Give the position of every Plasmodium parasite visible.
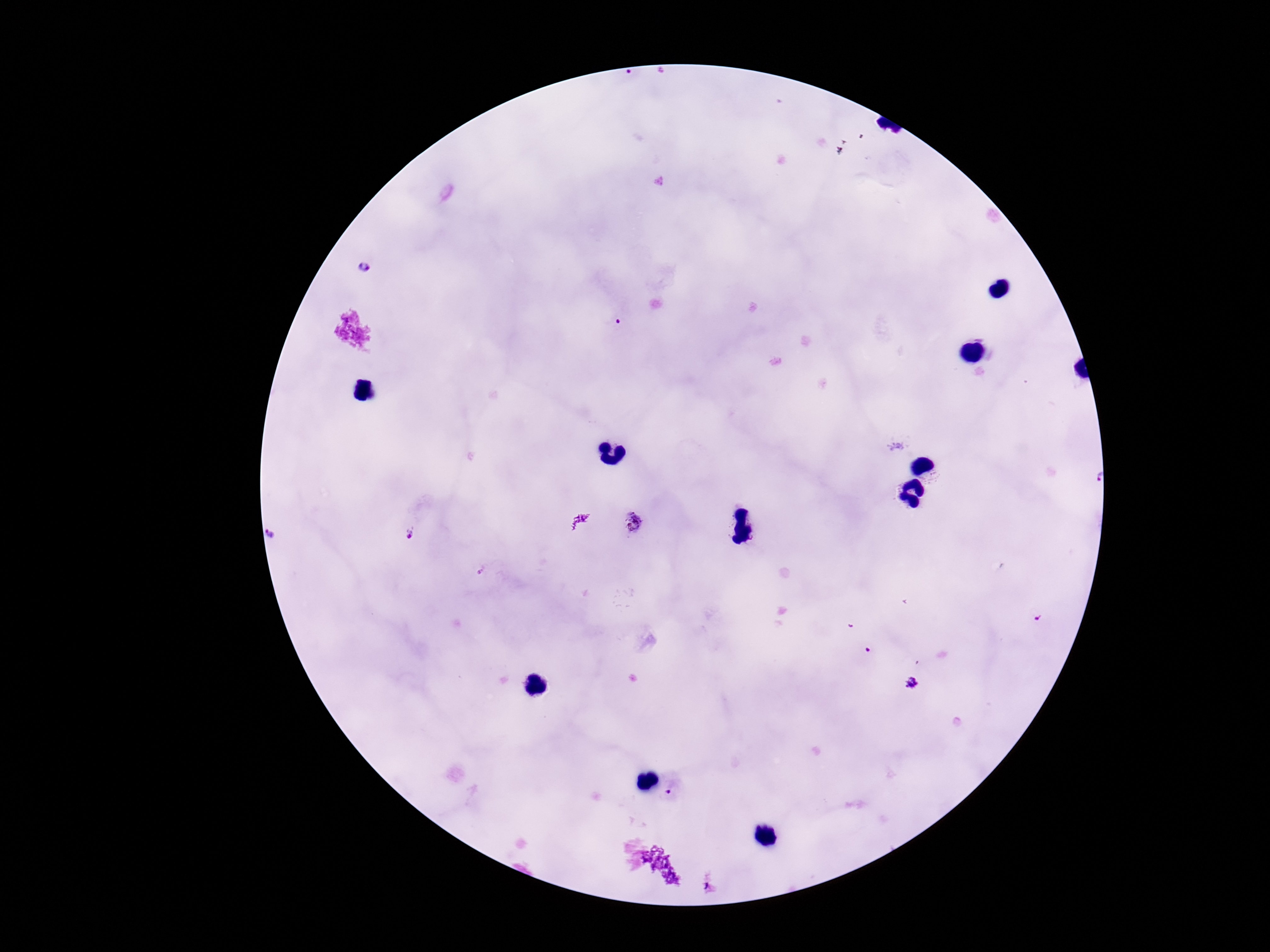
Approximate centers as (x, y) in pixels.
Plasmodium parasites: (363, 268), (619, 322), (1092, 478), (634, 523), (410, 533), (867, 651), (912, 682), (672, 789).

Smartphone photograph taken through the microscope eyepiece. Image is 1270×952 pixels. Giemsa-stained preparation. Thick peripheral-blood smear. One field from this slide. 100x magnification. Patient malaria status: positive.